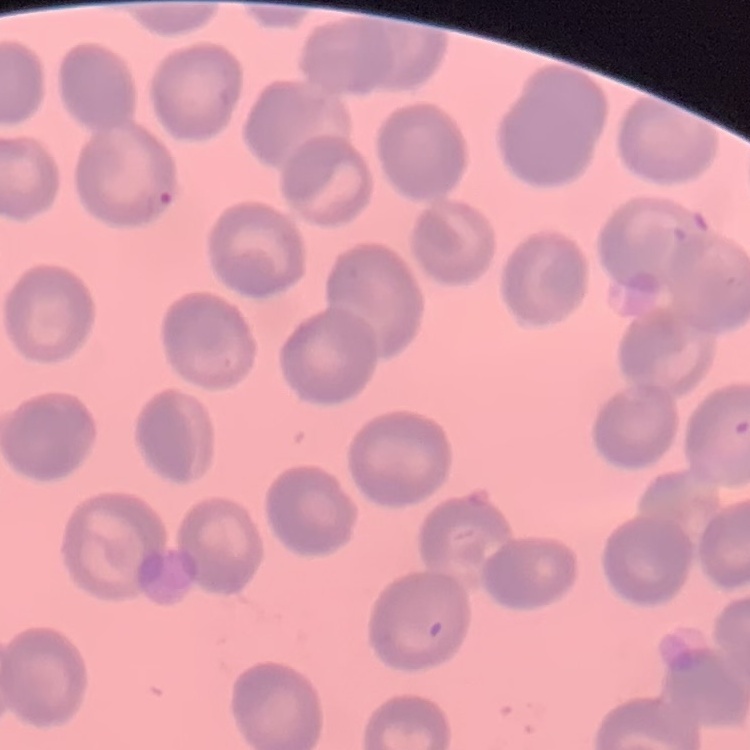
Summary:
  - Erythrocyte morphology: no rouleaux formation
  - Image type: square crop of a larger photomicrograph
  - Stain: Field's or Giemsa
  - Preparation: thin peripheral smear